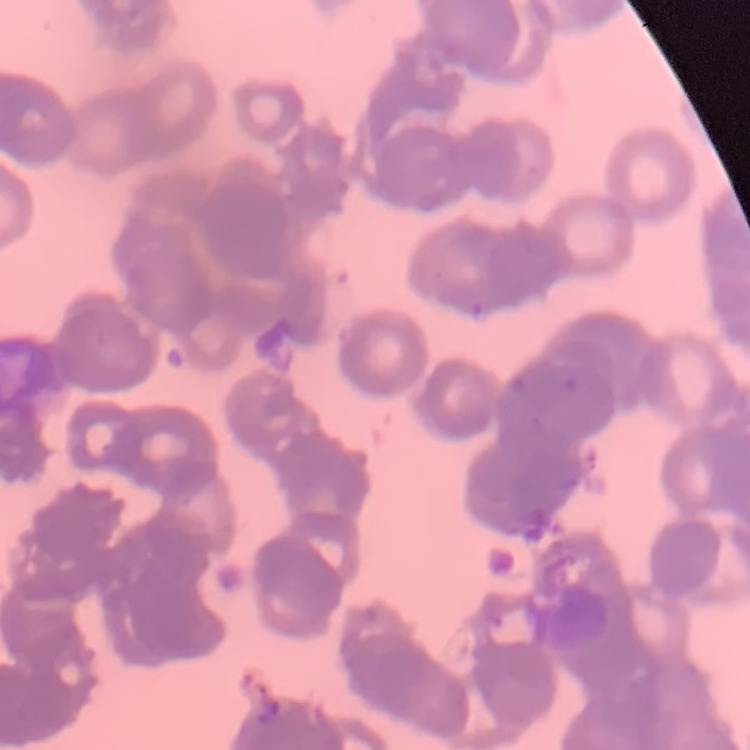
The erythrocytes show rouleaux formation. Field's or Giemsa stain. Thin peripheral smear. Square crop of a larger photomicrograph.